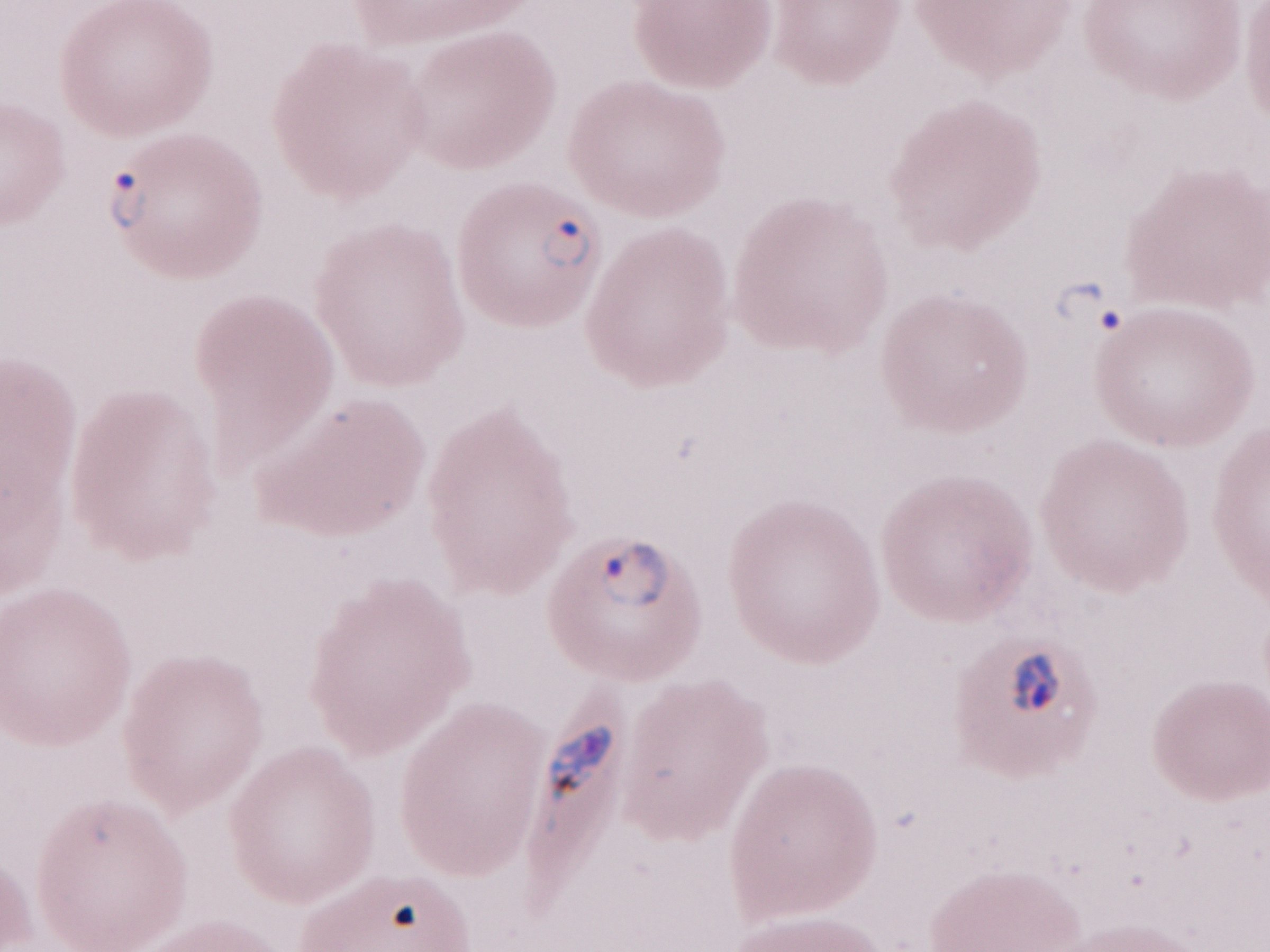

Olympus BX43 microscope, Olympus DP73 camera. Image is 1270×952 pixels. Magnification: 1,000x. Thin blood smear. Patient diagnosis: malaria infection. Single field of view. May-Grünwald-Giemsa-stained preparation.